Outline each blood parasite and name the species.
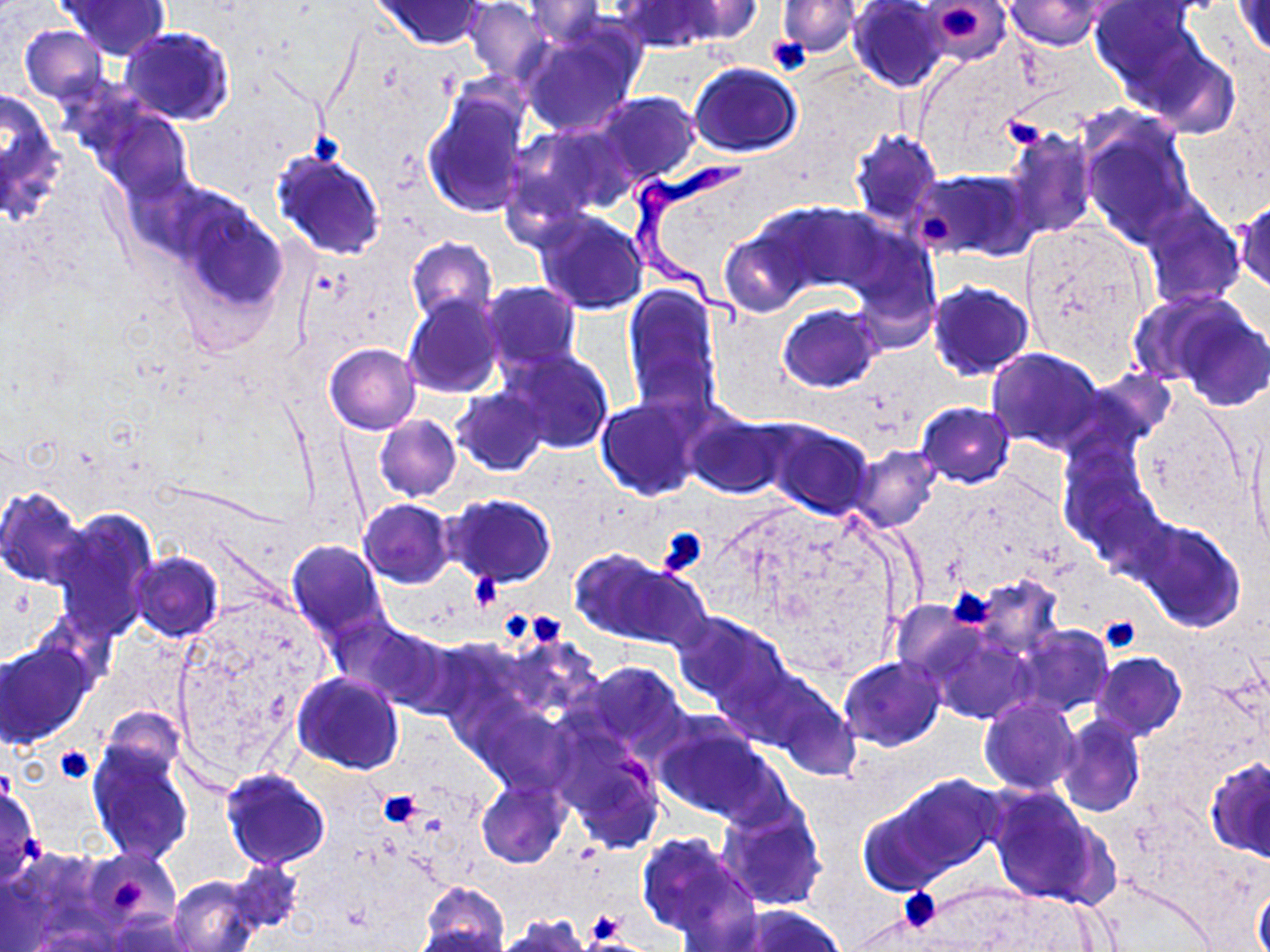
Approximate bounding boxes as (x1,y1)-(x2,y2) corner pairs in pixels.
Trypanosoma brucei: (624,159)-(759,331).
No Plasmodium falciparum, Plasmodium ovale, Plasmodium malariae, Plasmodium vivax, or Babesia divergens observed.

Uninfected red blood cell locations: (59,0)-(171,60), (375,0)-(487,49), (675,0)-(763,42), (849,0)-(949,92), (924,0)-(1010,63), (464,1)-(552,83), (524,1)-(607,48), (778,1)-(859,58), (1008,1)-(1103,50), (1090,1)-(1204,92), (1235,1)-(1270,58), (615,2)-(721,52), (19,25)-(109,105), (520,25)-(642,136), (121,27)-(234,125), (1141,44)-(1241,136), (690,63)-(802,158), (422,85)-(531,219), (1,87)-(64,217), (593,91)-(699,187), (79,96)-(195,202), (1077,113)-(1198,243), (1183,124)-(1269,223), (505,125)-(629,228), (1004,128)-(1098,242), (849,129)-(941,227), (269,146)-(387,260), (915,170)-(1034,261), (165,194)-(288,325), (1237,199)-(1269,295), (1140,201)-(1245,309), (775,203)-(887,299), (534,209)-(648,315), (1021,222)-(1153,364), (718,228)-(813,317), (849,228)-(942,347), (405,238)-(497,326), (481,281)-(581,374), (926,281)-(1034,381), (622,283)-(721,413), (1127,291)-(1242,387), (403,294)-(504,397), (1165,298)-(1270,411), (777,305)-(882,393), (325,343)-(420,434), (987,347)-(1106,452), (501,348)-(614,455), (453,388)-(548,476), (597,398)-(702,500), (916,401)-(1016,486), (685,411)-(789,499), (374,414)-(461,500), (761,420)-(873,520), (1246,429)-(1268,556), (1001,436)-(1072,507), (848,444)-(941,533), (1057,447)-(1161,566), (0,486)-(90,588), (445,495)-(556,586), (359,499)-(455,588), (50,511)-(157,640), (1134,518)-(1246,630), (286,541)-(390,641), (568,549)-(683,643), (128,552)-(224,643), (967,576)-(1064,659), (891,602)-(980,684), (674,611)-(791,713), (337,620)-(454,711), (1013,625)-(1115,717), (929,632)-(1032,725), (0,641)-(95,748), (1091,651)-(1186,741), (840,656)-(946,751), (578,661)-(687,753), (291,672)-(404,775), (749,675)-(860,777), (980,698)-(1081,794), (474,704)-(579,795), (102,709)-(186,780), (653,715)-(779,824), (1056,715)-(1145,816), (554,731)-(667,852), (86,740)-(193,864), (1205,758)-(1269,859), (220,769)-(331,870), (883,775)-(1004,882), (477,781)-(569,868), (0,783)-(41,882), (987,788)-(1111,909), (716,799)-(828,911), (857,804)-(952,894), (636,831)-(753,944), (86,851)-(180,934), (227,860)-(303,933), (168,875)-(261,952), (1254,882)-(1270,952), (419,883)-(509,952), (723,905)-(846,952), (105,914)-(199,951), (498,917)-(591,951), (407,924)-(504,952). Platelet locations: (936,5)-(985,44), (769,37)-(809,73), (1004,114)-(1048,149), (310,129)-(342,165), (919,214)-(953,246), (660,530)-(710,575), (472,574)-(498,604), (947,588)-(995,629), (528,610)-(563,645), (504,613)-(528,641), (1100,617)-(1139,653), (54,747)-(95,783), (378,789)-(422,827), (110,877)-(146,915), (896,888)-(941,929), (586,912)-(627,944). Slide-level diagnosis: Trypanosoma brucei. 1000x magnification. Thin blood film. Single field of view. Image is 1270×952 pixels. May-Grünwald-Giemsa stain. Optical microscopy.